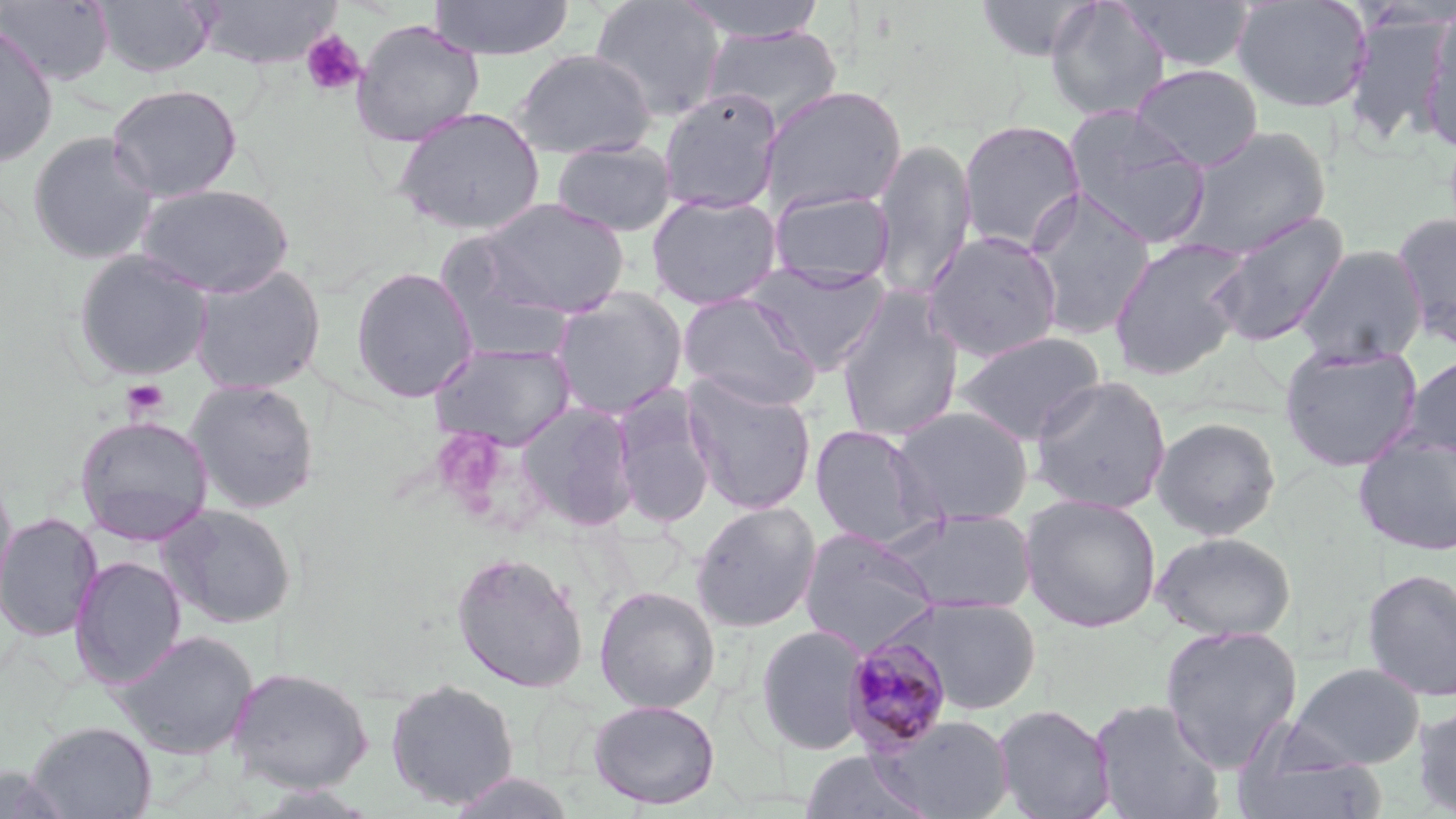

Approximate bounding boxes as (x1,y1)-(x2,y2) corner pairs in pixels. Plasmodium malariae-infected red blood cell locations: (843,633)-(955,756). Uninfected red blood cell locations: (0,0)-(114,86), (94,0)-(217,78), (193,0)-(341,69), (428,0)-(575,60), (589,0)-(727,122), (676,0)-(830,43), (973,0)-(1102,62), (1044,0)-(1170,122), (1117,0)-(1255,73), (1232,0)-(1373,113), (1342,9)-(1452,149), (1420,12)-(1456,151), (351,19)-(485,146), (0,23)-(59,168), (702,25)-(843,130), (511,48)-(656,160), (1131,64)-(1264,171), (106,83)-(242,201), (760,85)-(908,215), (657,90)-(782,213), (392,105)-(546,235), (1062,106)-(1212,250), (958,119)-(1086,253), (1178,126)-(1331,258), (27,131)-(159,265), (551,138)-(678,237), (871,139)-(977,300), (135,184)-(294,298), (768,188)-(896,288), (1022,188)-(1156,339), (645,192)-(783,310), (470,198)-(632,320), (1208,211)-(1349,347), (1392,211)-(1456,350), (922,230)-(1064,362), (1107,237)-(1249,381), (1294,245)-(1427,366), (433,247)-(579,365), (72,249)-(214,382), (746,262)-(890,373), (188,263)-(327,395), (349,266)-(479,403), (552,287)-(689,418), (677,291)-(822,411), (835,292)-(964,444), (954,330)-(1106,444), (430,341)-(576,450), (1279,342)-(1423,472), (1402,353)-(1456,459), (681,372)-(817,515), (1029,375)-(1172,514), (185,378)-(321,515), (609,387)-(718,530), (515,402)-(640,533), (893,405)-(1034,526), (74,415)-(215,545), (1151,417)-(1282,539), (809,423)-(943,551), (1353,431)-(1456,557), (0,469)-(18,618), (1020,494)-(1162,633), (691,501)-(822,633), (160,503)-(298,629), (888,509)-(1036,615), (0,512)-(102,642), (799,528)-(940,656), (1152,532)-(1295,640), (451,551)-(589,693), (70,556)-(186,690), (1361,568)-(1456,702), (594,585)-(720,713), (890,595)-(1041,714), (756,624)-(871,755), (1159,624)-(1303,772), (112,629)-(259,760), (1288,662)-(1425,769), (227,666)-(374,793), (385,677)-(520,809), (1089,697)-(1225,819), (587,698)-(721,809), (1412,702)-(1456,816), (991,703)-(1115,819), (871,713)-(1015,819), (26,721)-(157,819), (1232,737)-(1387,819), (797,751)-(934,818), (1,764)-(73,819), (446,772)-(577,818). Platelet locations: (301,30)-(366,97), (120,378)-(170,422). Slide-level diagnosis: Plasmodium malariae. Image is 1456×819 pixels. Captured at 1000x magnification. Optical microscopy. May-Grünwald-Giemsa-stained preparation. One field of a larger specimen. Thin blood film.